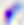

magnification = 400x
identification = Toxoplasma gondii
modality = photomicrograph